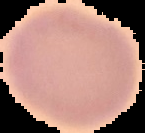

Summary:
  - Image size: 145×133 pixels
  - Result: negative for Plasmodium parasites
  - Preparation: thin blood smear
  - Image type: segmented cell region with the area outside set to black